State which parasite is depicted.
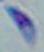
Toxoplasma gondii.

Summary:
  - Modality: photomicrograph
  - Magnification: 1000x